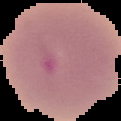 Result: no malaria parasites seen. From a thin blood film. Image is 121×121 pixels. The area outside the segmented cell region is set to black.